State the blood parasite species.
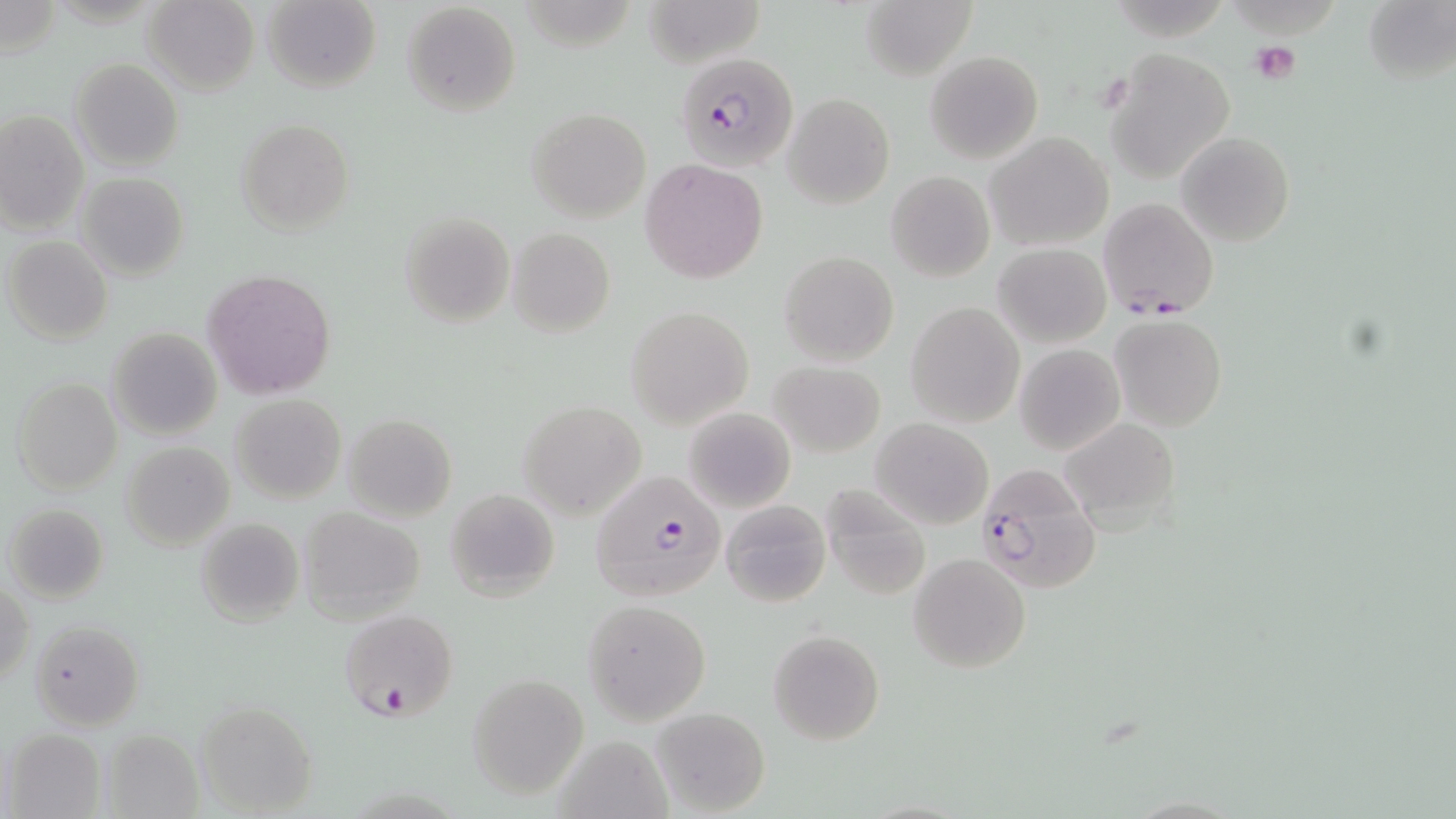
Plasmodium falciparum.

platelet locations = approximate bounding boxes as (x1,y1)-(x2,y2) corner pairs in pixels: (1248,41)-(1302,85)
Plasmodium falciparum-infected red blood cell locations = approximate bounding boxes as (x1,y1)-(x2,y2) corner pairs in pixels: (676,52)-(799,173), (1099,197)-(1218,319), (974,463)-(1102,594), (591,473)-(724,601), (339,609)-(460,722)
preparation = thin blood film
field of view = one of a larger specimen
uninfected red blood cell locations = approximate bounding boxes as (x1,y1)-(x2,y2) corner pairs in pixels: (141,0)-(259,94), (262,0)-(382,94), (643,0)-(765,69), (861,1)-(976,81), (1361,1)-(1454,85), (400,2)-(521,116), (1106,49)-(1236,183), (925,50)-(1043,164), (69,58)-(184,171), (781,92)-(896,208), (527,107)-(651,224), (0,111)-(90,237), (236,119)-(354,235), (1175,130)-(1296,247), (984,131)-(1114,249), (640,159)-(767,282), (886,170)-(995,282), (77,172)-(189,281), (398,211)-(515,328), (509,228)-(613,336), (4,235)-(114,345), (994,244)-(1110,347), (780,251)-(898,366), (202,270)-(336,399), (906,301)-(1025,427), (625,307)-(755,429), (1110,314)-(1227,432), (106,327)-(224,441), (1014,343)-(1124,454), (769,361)-(886,457), (11,377)-(123,496), (230,393)-(347,504), (518,400)-(647,518), (683,405)-(796,513), (342,413)-(458,521), (1061,417)-(1181,532), (871,418)-(993,530), (120,441)-(234,549), (825,486)-(930,602), (445,487)-(560,601), (720,499)-(832,607), (5,504)-(108,604), (297,507)-(425,619), (194,517)-(304,628), (909,554)-(1032,674), (1,581)-(33,688), (581,600)-(711,723), (30,620)-(145,732), (769,629)-(885,745), (467,673)-(589,799), (193,700)-(320,815), (650,706)-(769,816), (101,727)-(203,819), (6,728)-(105,817), (548,733)-(678,819)
stain = May-Grünwald-Giemsa
image size = 1456×819 pixels
magnification = 1000x
modality = light microscopy